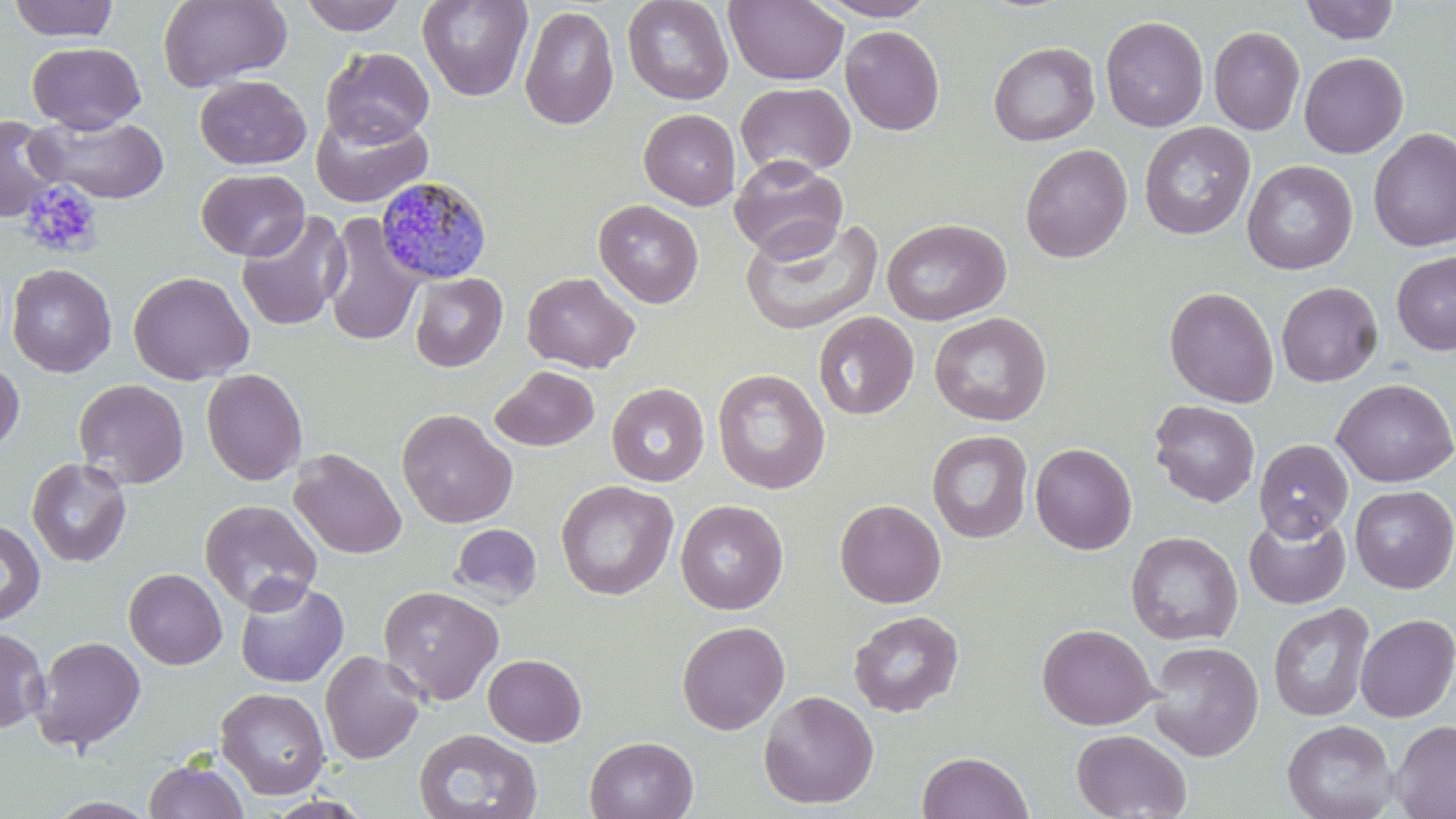 Approximate bounding boxes as (x1,y1)-(x2,y2) corner pairs in pixels. Plasmodium malariae-infected red blood cell locations: (375,176)-(492,285). Uninfected red blood cell locations: (6,0)-(120,42), (158,0)-(292,91), (298,0)-(407,36), (417,0)-(533,102), (622,0)-(734,105), (724,0)-(849,86), (814,0)-(938,21), (1299,0)-(1400,45), (519,5)-(619,130), (1100,16)-(1209,133), (840,25)-(945,135), (1208,26)-(1305,135), (27,41)-(145,133), (988,41)-(1100,146), (321,47)-(434,147), (1298,52)-(1408,158), (195,75)-(311,170), (735,82)-(856,179), (639,108)-(741,210), (310,109)-(433,207), (0,114)-(61,223), (28,115)-(170,204), (1139,122)-(1255,240), (1368,127)-(1456,252), (1020,143)-(1133,263), (729,156)-(848,261), (1242,159)-(1358,274), (196,168)-(309,261), (594,199)-(704,308), (235,211)-(350,332), (322,213)-(424,348), (740,217)-(885,336), (881,217)-(1011,326), (1392,252)-(1456,356), (7,263)-(117,377), (128,271)-(255,385), (522,271)-(640,374), (410,272)-(507,372), (1276,281)-(1383,387), (1164,286)-(1279,408), (813,311)-(919,420), (929,312)-(1051,426), (0,358)-(25,453), (490,365)-(600,451), (201,369)-(308,485), (712,369)-(830,494), (73,378)-(190,489), (1332,378)-(1456,487), (606,382)-(709,486), (1150,399)-(1260,507), (396,408)-(518,529), (926,430)-(1033,543), (1254,439)-(1353,541), (1030,443)-(1137,555), (288,448)-(406,559), (26,457)-(132,567), (555,480)-(678,600), (1350,485)-(1456,593), (199,498)-(323,614), (834,498)-(946,608), (675,499)-(788,614), (1244,513)-(1350,609), (0,520)-(46,625), (450,523)-(542,604), (1126,531)-(1243,646), (123,568)-(228,669), (234,577)-(349,689), (378,585)-(504,706), (1268,602)-(1374,722), (848,610)-(964,717), (1355,614)-(1456,722), (677,620)-(790,735), (1037,623)-(1158,730), (0,626)-(49,733), (31,636)-(146,752), (1146,641)-(1264,762), (320,649)-(425,764), (483,654)-(586,747), (216,687)-(330,799), (759,690)-(879,810), (1282,719)-(1397,819), (1390,719)-(1456,819), (414,728)-(542,819), (1072,729)-(1192,818), (584,735)-(698,819), (916,751)-(1033,819), (144,759)-(250,819), (46,796)-(159,818). Platelet locations: (19,181)-(103,259). Slide-level diagnosis: Plasmodium malariae. 1000x magnification. May-Grünwald-Giemsa-stained preparation. Thin blood smear. One field of a larger specimen. Image is 1456×819 pixels. Optical microscopy.